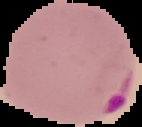

result: Plasmodium parasites detected
preparation: thin blood smear
image_type: segmented cell region on a black background
image_size: 142×127 pixels